Locate every malaria parasite.
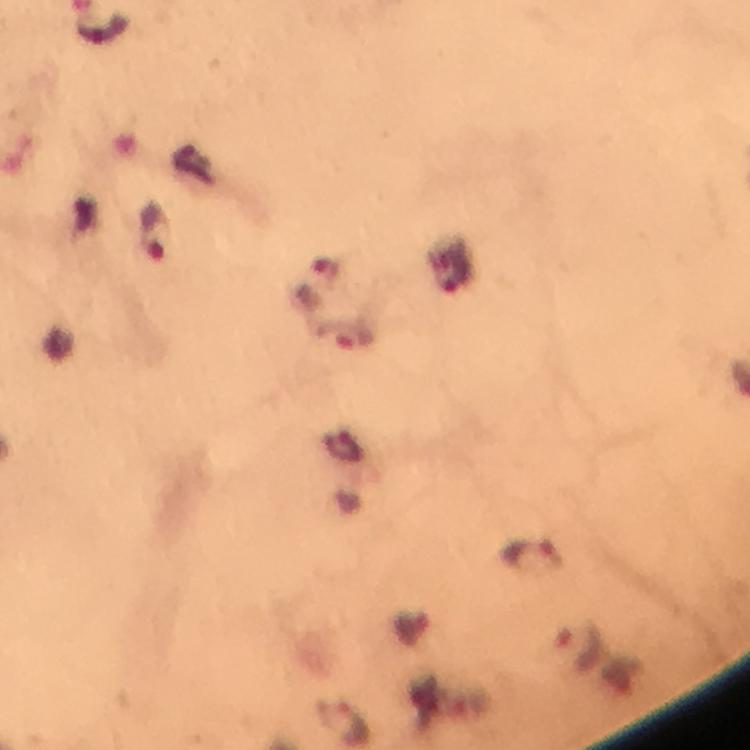

Approximate centers as [x, y] in pixels.
Malaria parasites: [103, 31], [157, 234], [459, 276], [347, 337], [533, 556], [577, 646].

Summary:
  - Capture: smartphone camera through the microscope
  - Magnification: 100x
  - Stain: Giemsa
  - Context: from a diagnostic examination for malaria
  - Preparation: thick smear
  - Immersion oil: applied
  - Image size: 750×750 pixels
  - Cropped from: one field of view